Identify the cell.
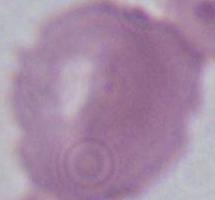
This is an erythrocyte.

Summary:
  - Magnification: 1000x
  - Modality: photomicrograph